State the preparation type.
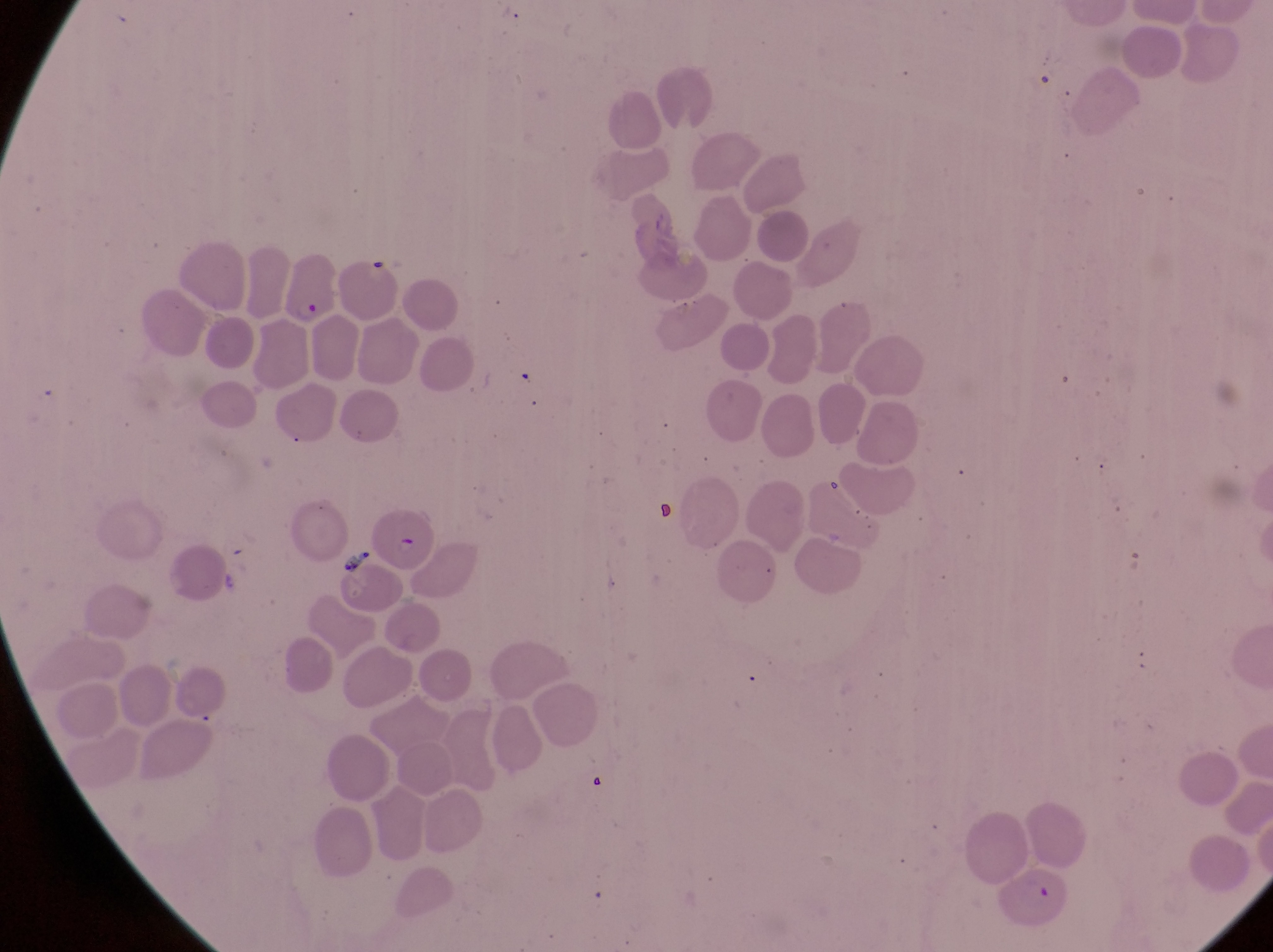

Thin blood film.

Approximate bounding boxes as (left, top, right, bottom) in pixels.
Summary:
  - Artifact (platelet-like body, stain precipitate, or debris) locations: (335, 544, 377, 581)
  - Parasitised red blood cell locations: (278, 250, 341, 327), (1001, 867, 1074, 923)
  - Capture: smartphone photograph through the eyepiece of an Olympus CX-23 microscope
  - Image size: 1273×952 pixels
  - Magnification: 1000x
  - Country: Uganda
  - Field of view: single